Name the parasite shown.
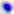
This is Toxoplasma gondii.

{
  "magnification": "400x",
  "modality": "photomicrograph"
}